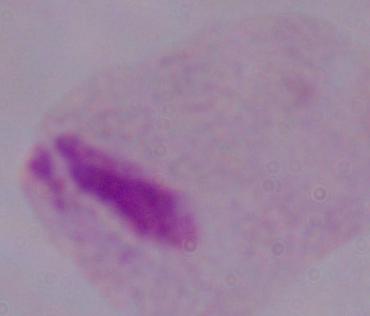

A trichomonad is shown. Photomicrograph. 1000x magnification.